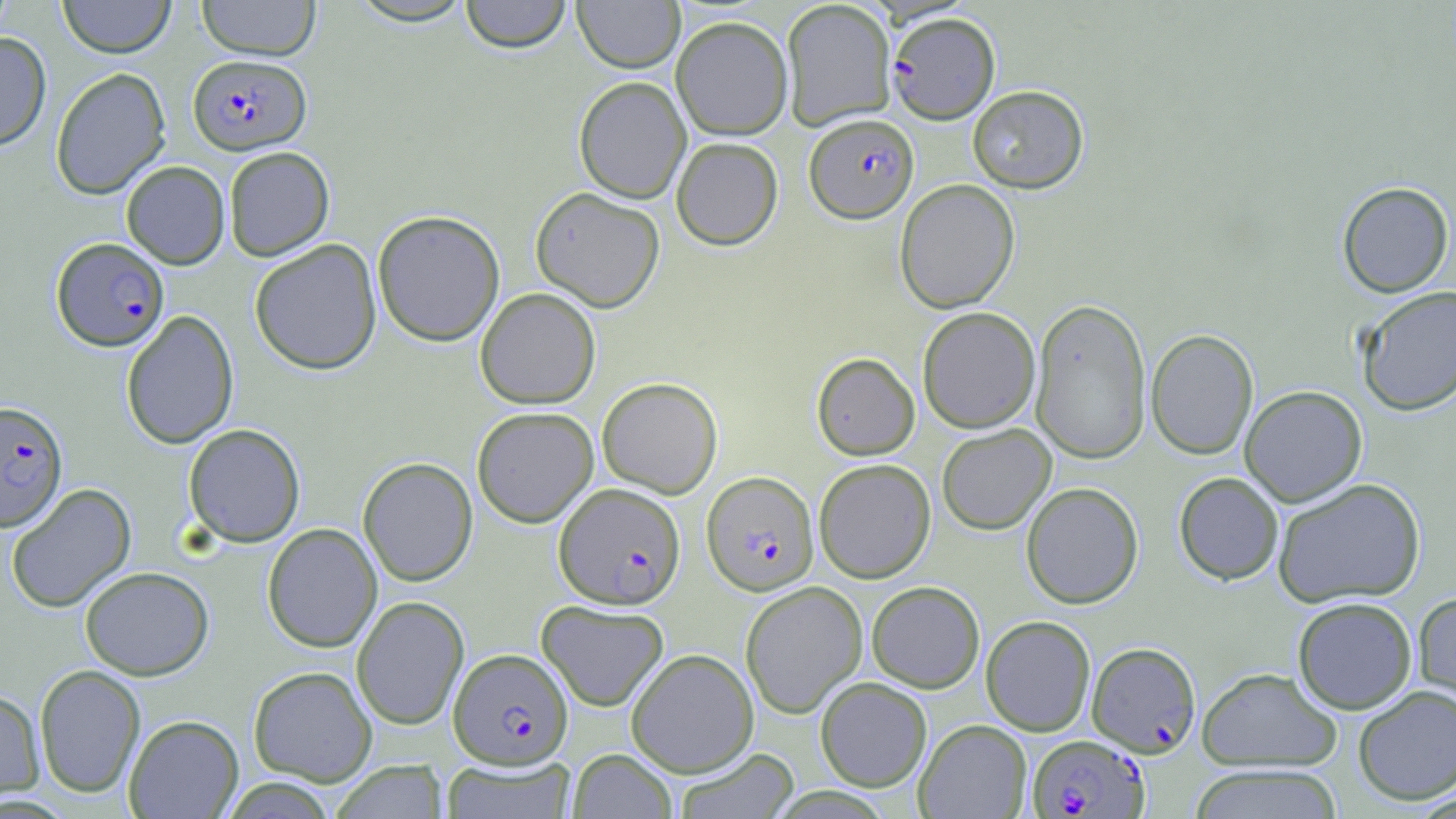
{
  "slide_level_diagnosis": "Plasmodium falciparum",
  "image_size": "1456×819 pixels",
  "field_of_view": "one of a larger specimen",
  "plasmodium_falciparum_infected_red_blood_cell_locations": "approximate bounding boxes as named x1/y1/x2/y2 corners in pixels: (x1=887, y1=12, x2=1000, y2=124), (x1=188, y1=54, x2=310, y2=155), (x1=805, y1=114, x2=919, y2=222), (x1=52, y1=237, x2=169, y2=351), (x1=0, y1=400, x2=68, y2=532), (x1=701, y1=471, x2=819, y2=595), (x1=554, y1=483, x2=685, y2=609), (x1=1087, y1=641, x2=1201, y2=757), (x1=449, y1=648, x2=573, y2=768), (x1=1027, y1=734, x2=1148, y2=818)",
  "preparation": "thin blood smear",
  "uninfected_red_blood_cell_locations": "approximate bounding boxes as named x1/y1/x2/y2 corners in pixels: (x1=0, y1=0, x2=16, y2=42), (x1=58, y1=0, x2=175, y2=58), (x1=196, y1=0, x2=322, y2=61), (x1=347, y1=0, x2=477, y2=26), (x1=459, y1=0, x2=572, y2=53), (x1=573, y1=0, x2=684, y2=73), (x1=781, y1=0, x2=896, y2=131), (x1=671, y1=16, x2=793, y2=140), (x1=0, y1=32, x2=51, y2=150), (x1=50, y1=67, x2=170, y2=199), (x1=573, y1=77, x2=691, y2=203), (x1=967, y1=85, x2=1088, y2=193), (x1=671, y1=137, x2=784, y2=250), (x1=223, y1=146, x2=334, y2=261), (x1=121, y1=161, x2=230, y2=269), (x1=895, y1=179, x2=1020, y2=313), (x1=1336, y1=181, x2=1454, y2=298), (x1=530, y1=187, x2=665, y2=312), (x1=372, y1=210, x2=505, y2=346), (x1=249, y1=239, x2=382, y2=375), (x1=1356, y1=286, x2=1456, y2=415), (x1=475, y1=287, x2=601, y2=409), (x1=1030, y1=296, x2=1152, y2=464), (x1=917, y1=307, x2=1040, y2=433), (x1=121, y1=310, x2=239, y2=449), (x1=1146, y1=329, x2=1258, y2=460), (x1=811, y1=352, x2=920, y2=460), (x1=597, y1=377, x2=723, y2=498), (x1=1240, y1=385, x2=1367, y2=506), (x1=472, y1=406, x2=599, y2=527), (x1=183, y1=423, x2=306, y2=547), (x1=937, y1=424, x2=1056, y2=534), (x1=358, y1=457, x2=478, y2=586), (x1=814, y1=459, x2=936, y2=583), (x1=1173, y1=472, x2=1284, y2=585), (x1=1273, y1=477, x2=1426, y2=607), (x1=6, y1=482, x2=136, y2=613), (x1=1021, y1=482, x2=1144, y2=609), (x1=262, y1=523, x2=382, y2=653), (x1=80, y1=566, x2=214, y2=680), (x1=740, y1=581, x2=867, y2=718), (x1=866, y1=581, x2=985, y2=693), (x1=1412, y1=590, x2=1456, y2=717), (x1=352, y1=596, x2=469, y2=730), (x1=1292, y1=597, x2=1417, y2=714), (x1=536, y1=599, x2=669, y2=711), (x1=981, y1=615, x2=1096, y2=736), (x1=626, y1=648, x2=758, y2=778), (x1=34, y1=664, x2=145, y2=799), (x1=248, y1=665, x2=377, y2=787), (x1=1197, y1=667, x2=1342, y2=771), (x1=815, y1=676, x2=932, y2=792), (x1=1353, y1=684, x2=1456, y2=805), (x1=0, y1=689, x2=45, y2=802), (x1=124, y1=714, x2=244, y2=818), (x1=914, y1=719, x2=1032, y2=818), (x1=674, y1=747, x2=799, y2=819), (x1=568, y1=748, x2=677, y2=819), (x1=441, y1=757, x2=576, y2=819), (x1=332, y1=761, x2=447, y2=819), (x1=1188, y1=764, x2=1344, y2=818), (x1=218, y1=778, x2=338, y2=818)",
  "modality": "light microscopy",
  "magnification": "1000x",
  "stain": "May-Grünwald-Giemsa"
}